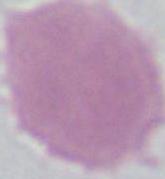

Summary:
  - Modality: photomicrograph
  - Magnification: 1000x
  - Identification: erythrocyte